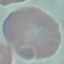
Malaria status: uninfected. Giemsa-stained preparation. Automatically extracted cell patch, resized to 64 × 64 pixels. Thin smear of blood. Acquired by smartphone through the microscope eyepiece.